Classify this cell by malaria status.
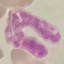

Uninfected.

Giemsa stain. Acquired by smartphone through the microscope eyepiece. Automatically extracted cell patch, resized to 64 × 64 pixels. Thin blood smear.